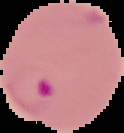
Summary:
  - Image size: 124×133 pixels
  - Image type: segmented cell region on a black background
  - Result: malaria parasites identified
  - Preparation: thin blood smear